State which parasite is depicted.
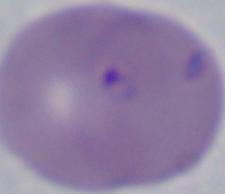

This is Babesia.

Micrograph. 1000x magnification.